Comment on the morphology of the erythrocytes.
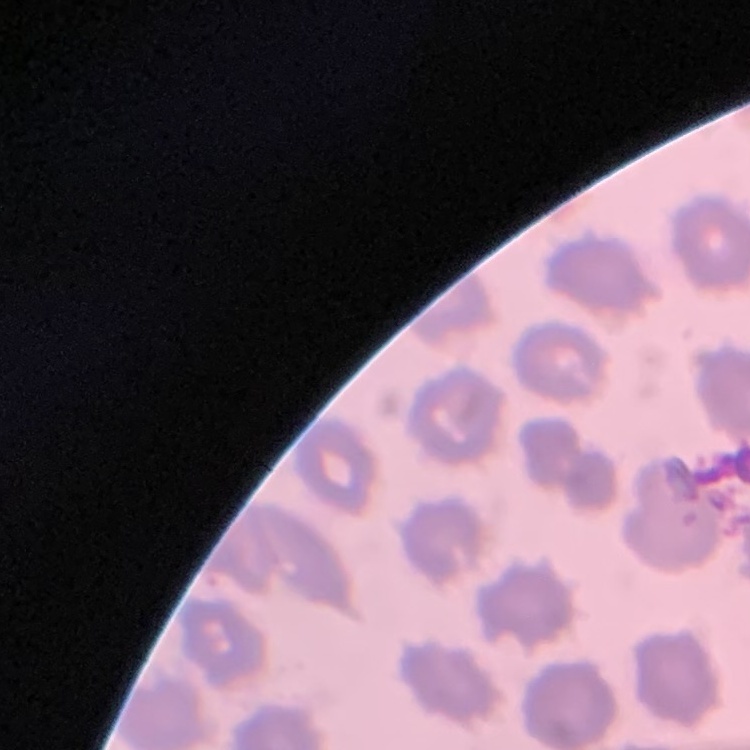

They show no rouleaux formation.

preparation = thin peripheral smear
stain = Field's or Giemsa
image type = square crop of a larger photomicrograph